Give the position of every Plasmodium parasite visible.
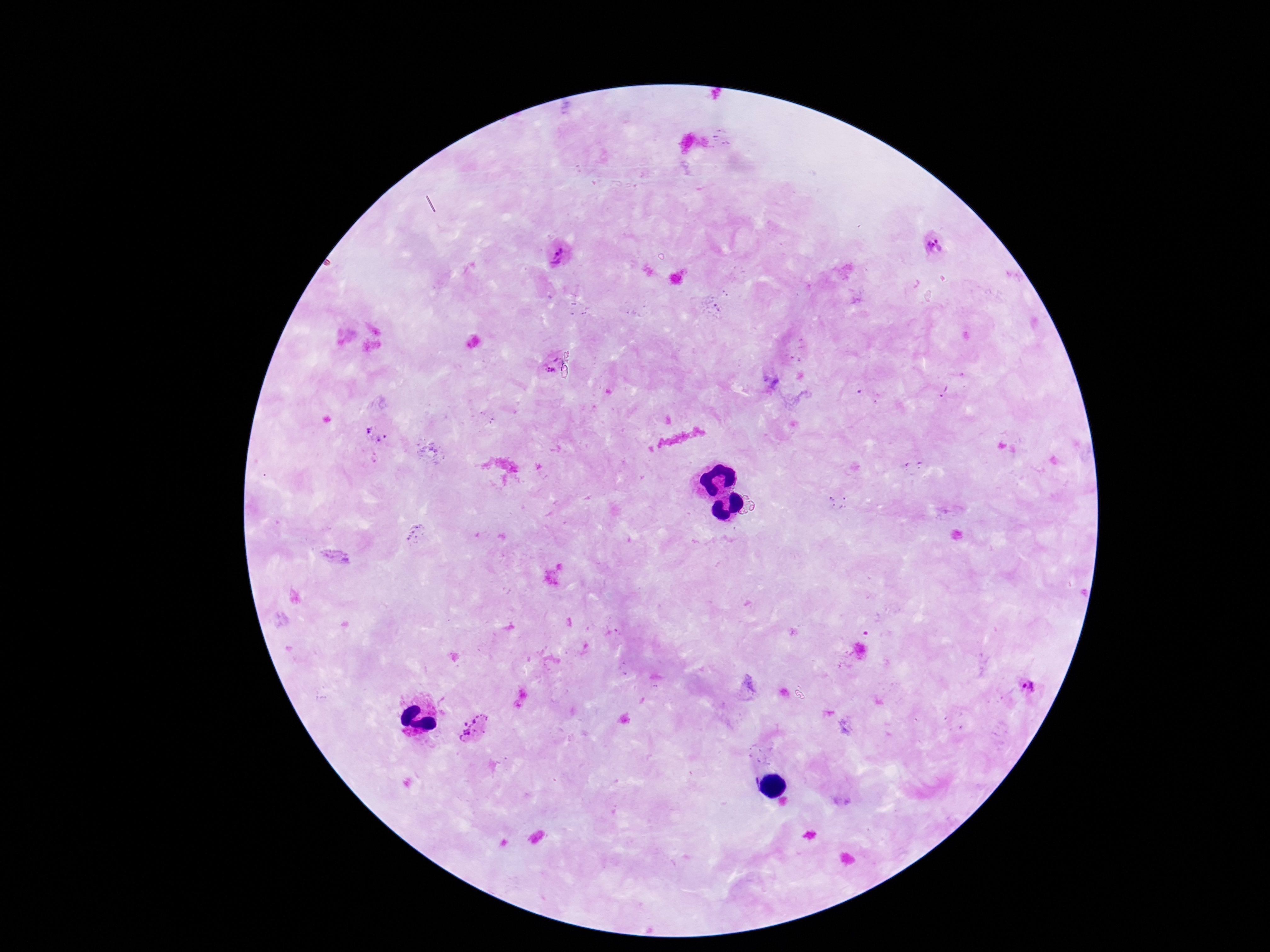

Approximate centers as [x, y] in pixels.
Plasmodium parasites: [934, 244], [560, 255], [552, 367], [944, 391], [376, 434], [1033, 686], [473, 727].

Summary:
  - Patient malaria status: positive
  - Magnification: 100x
  - Image size: 1270×952 pixels
  - Stain: Giemsa
  - Capture: smartphone camera through the microscope eyepiece
  - Preparation: thick peripheral-blood smear
  - Field of view: single